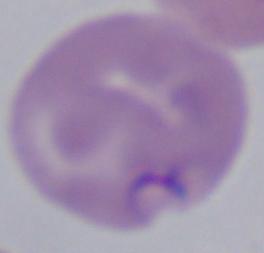

Summary:
  - Magnification: 1000x
  - Modality: photomicrograph
  - Identification: Babesia